Classify this cell by malaria status.
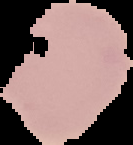

It is uninfected.

Summary:
  - Image type: segmented cell region on a black background
  - Preparation: thin blood film
  - Image size: 133×145 pixels